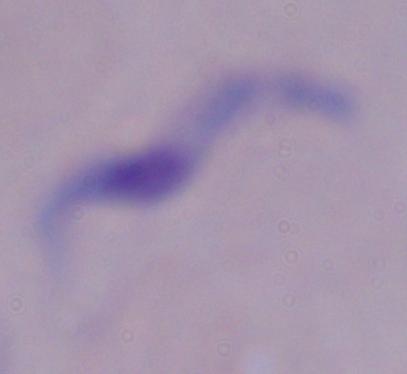

Captured at 1000x magnification. Micrograph. A trypanosome is seen.